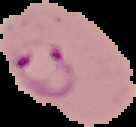
{
  "image_size": "136×127 pixels",
  "preparation": "thin blood film",
  "image_type": "segmented cell region with the area outside set to black",
  "result": "malaria parasites detected"
}